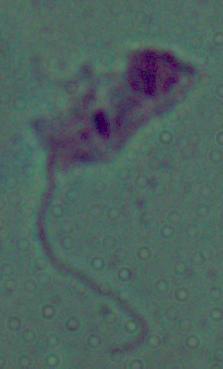

magnification: 1000x
modality: micrograph
identification: Leishmania